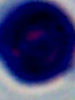
magnification = 1000x
identification = white blood cell
modality = micrograph